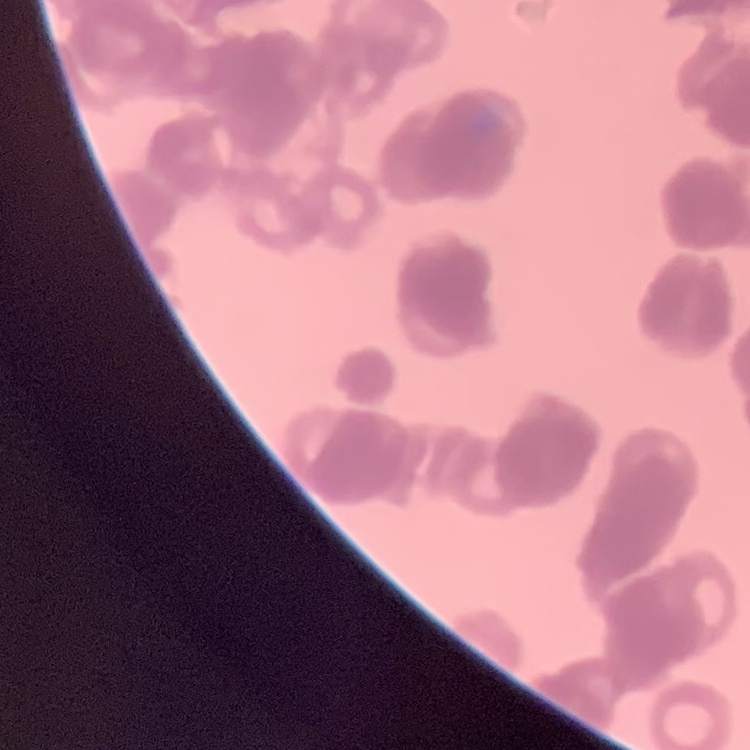
Summary:
  - Red blood cell morphology: rouleaux formation
  - Preparation: thin blood smear
  - Image type: square crop of a larger photomicrograph
  - Stain: Field's or Giemsa